Comment on the morphology of the erythrocytes.
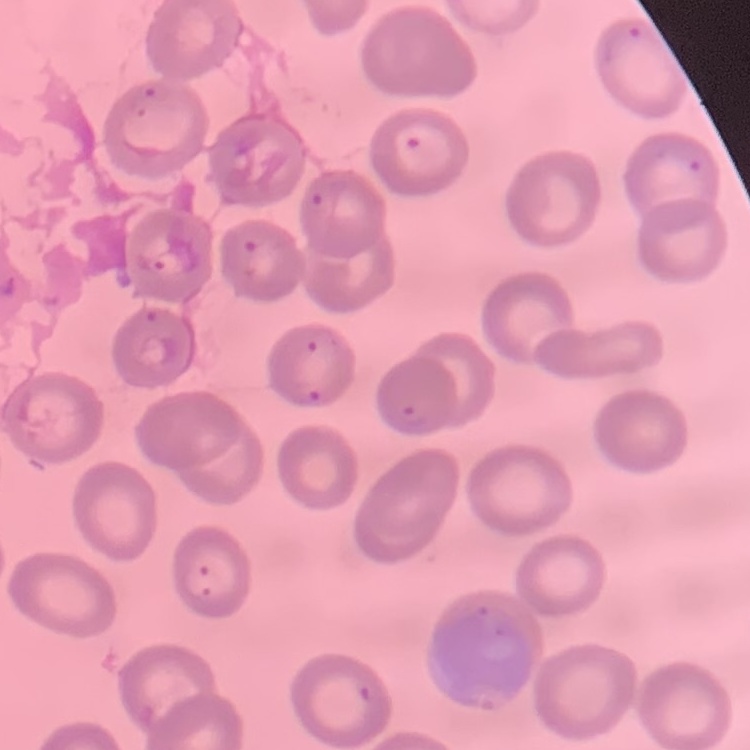

No rouleaux formation.

Summary:
  - Image type: square crop of a larger photomicrograph
  - Preparation: thin blood smear
  - Stain: Field's or Giemsa